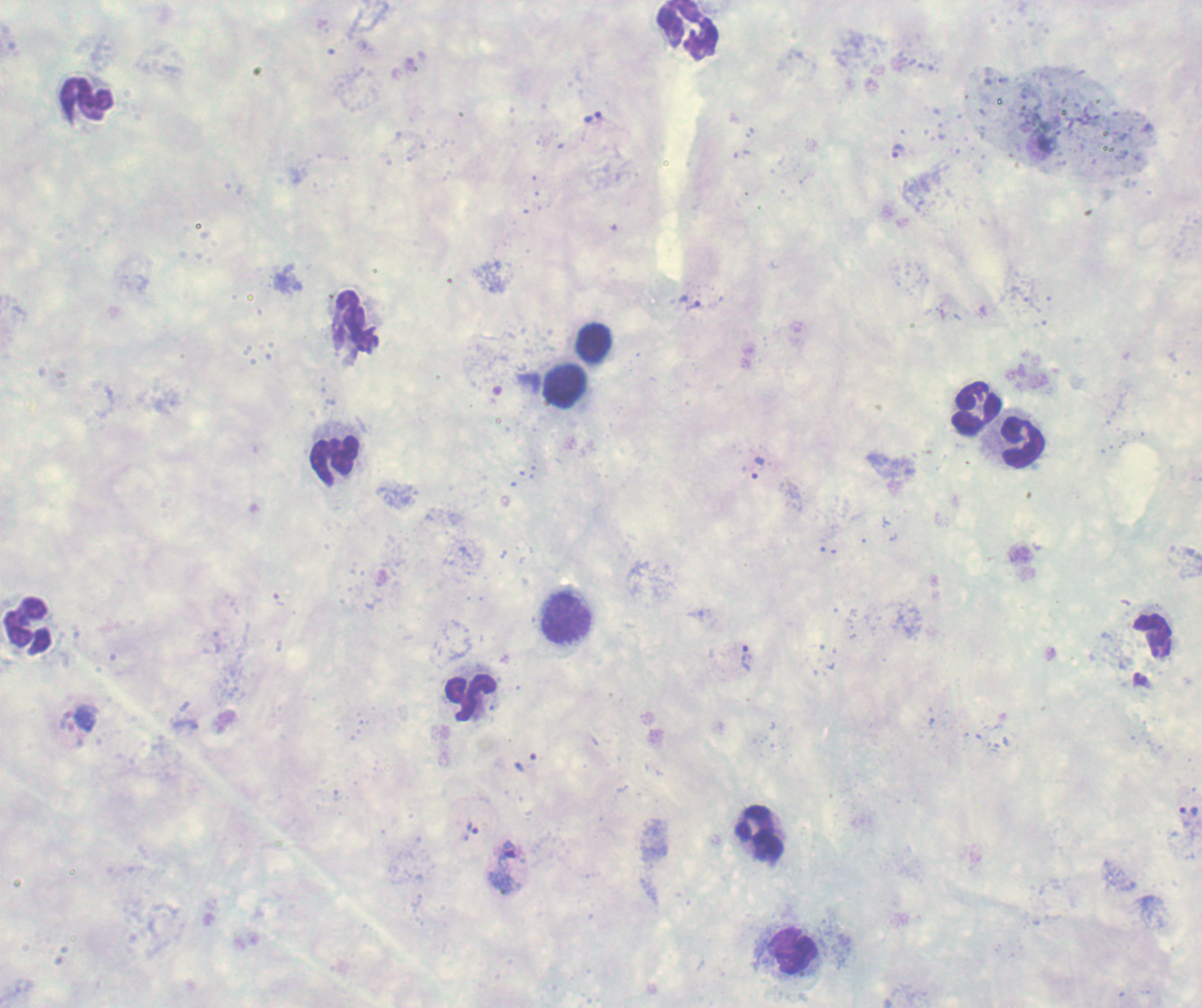

coordinate format = approximate object centers, in pixels from the top-left corner
gametocyte locations = (x=506, y=866)
trophozoite locations = (x=591, y=118), (x=897, y=151), (x=693, y=306), (x=758, y=467), (x=746, y=658), (x=1188, y=811), (x=471, y=832)
leukocyte locations = (x=688, y=30), (x=86, y=101), (x=353, y=323), (x=593, y=343), (x=564, y=386), (x=975, y=408), (x=1020, y=441), (x=333, y=460), (x=564, y=619), (x=28, y=626), (x=1153, y=637), (x=470, y=698), (x=761, y=833), (x=794, y=952)
life-cycle stages observed = trophozoite, gametocyte
field of view = single
preparation = thick blood film
stain = Romanowsky
image size = 1202×1008 pixels
background quality = poor
result = positive for malaria parasites
context = previously used in a real diagnosis
magnification = 100x